Assess this cell for malaria.
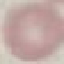

Uninfected.

Thin blood smear. Photographed with a smartphone camera at the microscope eyepiece. Cell patch, automatically extracted from a larger field of view and resized to 64 × 64 pixels. Giemsa-stained preparation.